Describe the morphology of the erythrocytes.
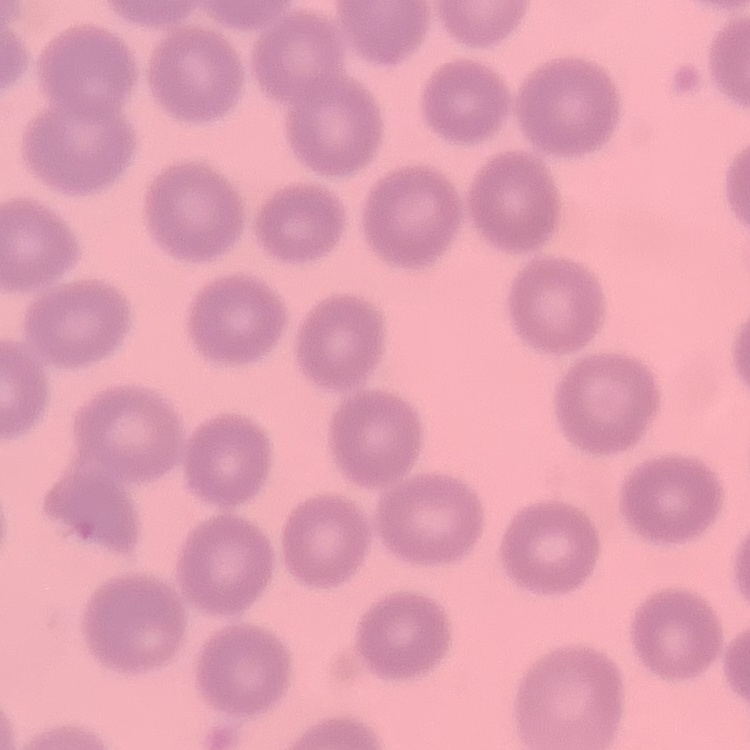
They show no rouleaux formation.

Square crop of a larger photomicrograph. Thin peripheral smear. Field's or Giemsa stain.